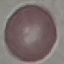
{
  "result": "no malaria parasites detected",
  "preparation": "thin smear",
  "stain": "Giemsa",
  "image_type": "cell patch, automatically extracted from a larger field of view and resized to 64 × 64 pixels",
  "capture": "smartphone through the microscope eyepiece"
}